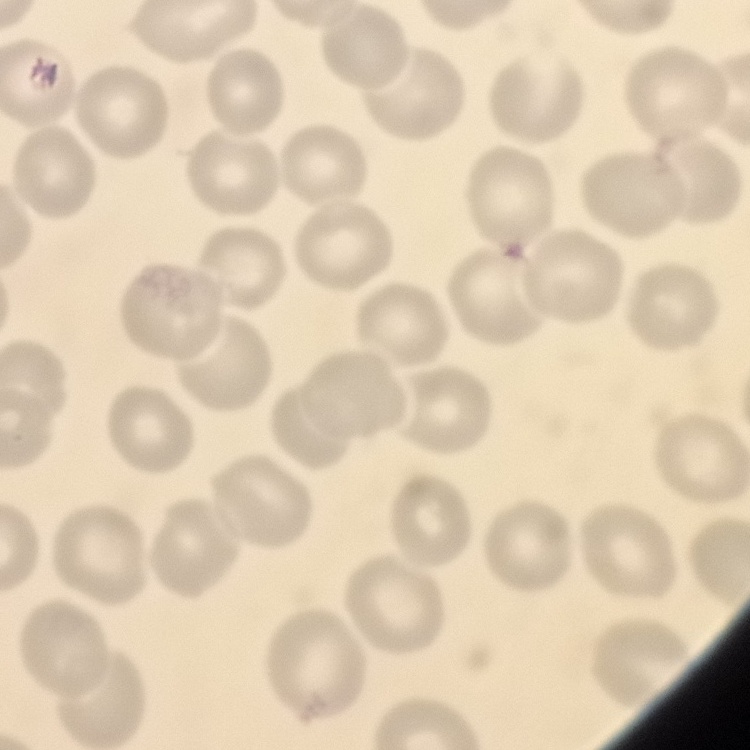 The red blood cells exhibit no rouleaux formation. Thin blood smear. Stained with either Field's or Giemsa. One tile cut from a larger photomicrograph.